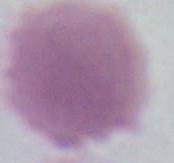
magnification: 1000x
identification: erythrocyte
modality: photomicrograph